Assess the morphology of the red blood cells.
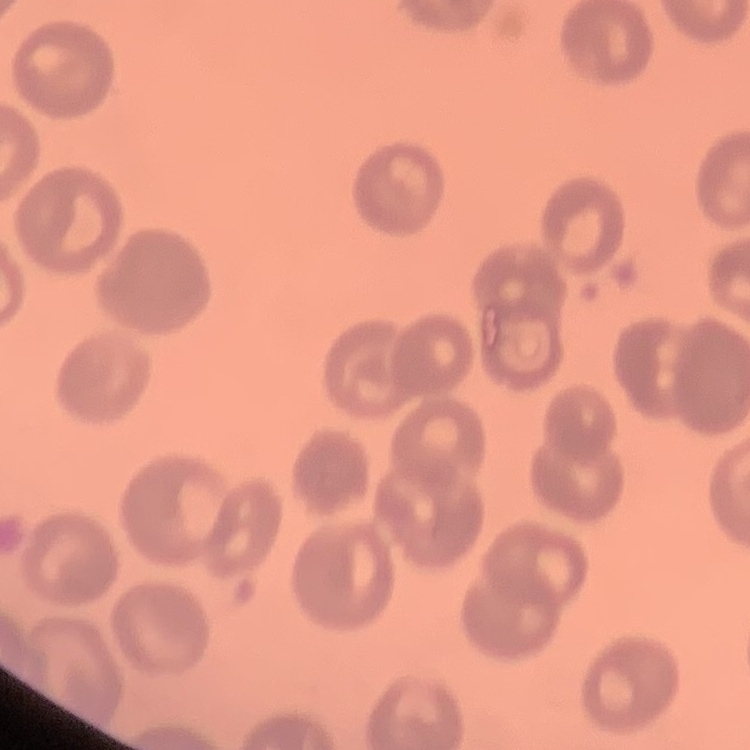

No rouleaux formation.

Thin blood smear. One tile cut from a larger photomicrograph. Stained with either Field's or Giemsa.